Assess this cell for malaria.
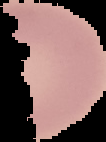

It is uninfected.

image type = cell region segmented out of the field of view; surrounding area masked to black
preparation = thin blood film
image size = 106×142 pixels